Report the malaria status of this cell.
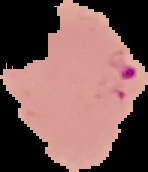

It is parasitized.

preparation = thin blood smear
image size = 148×172 pixels
image type = segmented cell region on a black background